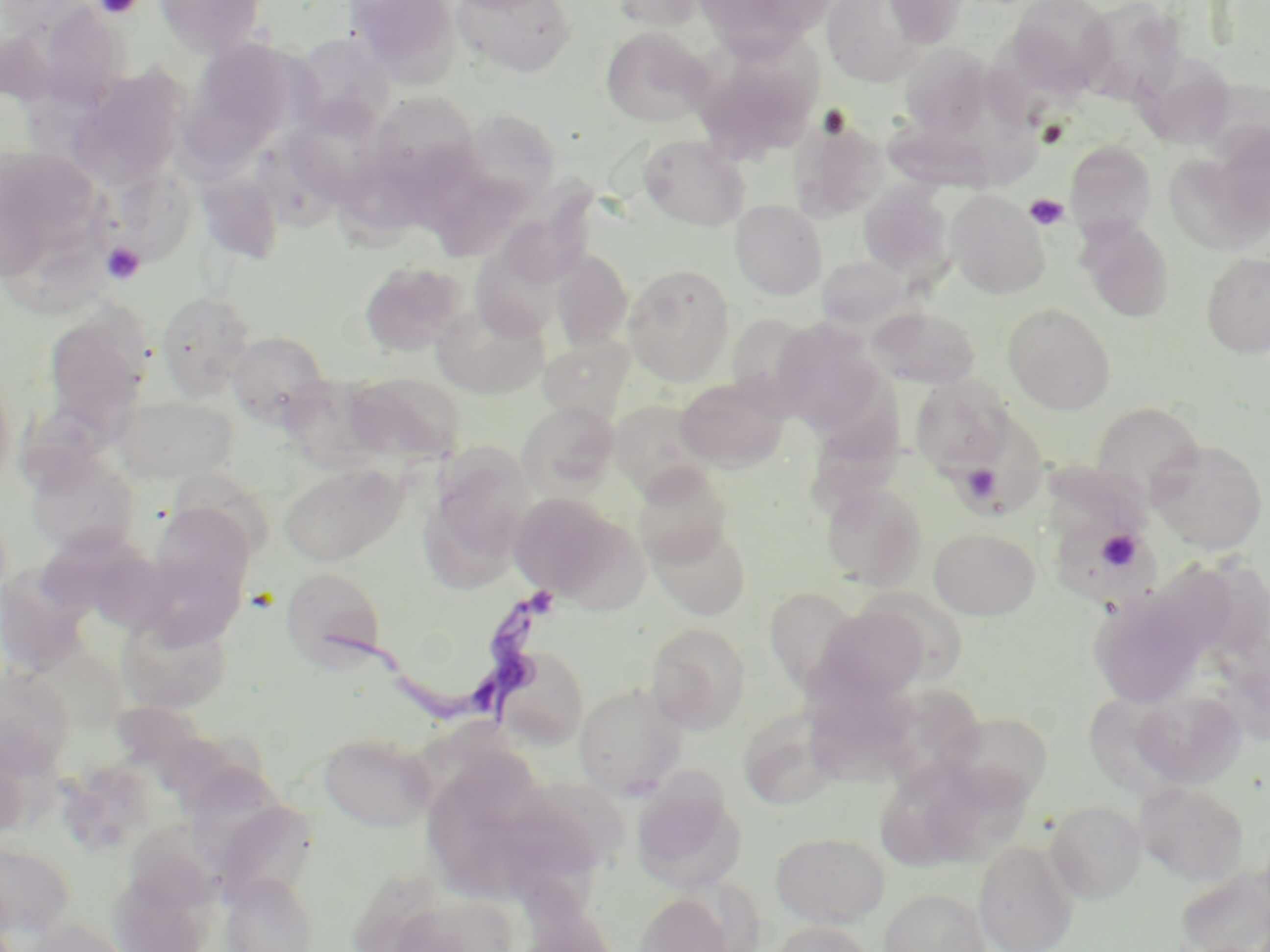
slide_level_diagnosis: Trypanosoma brucei
field_of_view: one of a larger specimen
magnification: 1000x
uninfected_red_blood_cell_locations: 'approximate bounding boxes as (x1, y1, x2, y2) in pixels: (153, 0, 267, 56), (345, 0, 462, 86), (452, 0, 576, 78), (611, 0, 707, 30), (694, 0, 829, 57), (821, 0, 925, 87), (884, 0, 971, 48), (1005, 0, 1115, 98), (1076, 0, 1185, 104), (600, 26, 711, 127), (691, 32, 825, 161), (290, 33, 395, 133), (192, 38, 307, 144), (899, 43, 997, 139), (1141, 58, 1237, 148), (71, 66, 190, 186), (365, 93, 481, 196), (284, 98, 388, 205), (459, 109, 560, 207), (790, 115, 890, 221), (638, 135, 750, 231), (1064, 141, 1157, 240), (0, 147, 109, 278), (1163, 151, 1264, 256), (109, 164, 197, 266), (197, 171, 285, 264), (858, 182, 954, 282), (947, 191, 1049, 298), (731, 200, 827, 300), (1078, 219, 1175, 322), (470, 236, 566, 342), (552, 250, 633, 350), (1201, 252, 1270, 358), (818, 256, 909, 330), (359, 261, 466, 356), (623, 264, 736, 386), (156, 291, 256, 398), (432, 303, 548, 399), (1004, 304, 1115, 413), (871, 306, 979, 389), (41, 307, 152, 439), (725, 313, 816, 406), (770, 318, 885, 434), (228, 331, 331, 427), (0, 362, 17, 490), (343, 373, 464, 468), (911, 375, 1016, 471), (675, 376, 789, 472), (113, 392, 239, 484), (802, 393, 907, 524), (609, 400, 714, 498), (518, 401, 620, 496), (1092, 401, 1205, 503), (1148, 440, 1268, 556), (426, 443, 534, 572), (24, 448, 140, 558), (278, 463, 406, 567), (631, 465, 731, 568), (174, 470, 274, 573), (820, 483, 927, 590), (509, 493, 634, 604), (147, 501, 255, 609), (650, 522, 751, 620), (1059, 522, 1163, 610), (929, 528, 1040, 620), (40, 533, 189, 634), (280, 566, 388, 671), (764, 587, 865, 694), (1089, 587, 1209, 709), (816, 604, 932, 706), (117, 608, 232, 713), (645, 623, 750, 733), (494, 645, 589, 749), (0, 667, 76, 775), (574, 683, 685, 799), (1131, 690, 1246, 788), (885, 691, 985, 792), (740, 711, 837, 811), (941, 711, 1053, 807), (318, 731, 436, 832), (428, 751, 550, 880), (631, 769, 745, 894), (506, 773, 628, 879), (1136, 782, 1249, 883), (1045, 800, 1146, 903), (216, 809, 320, 911), (125, 822, 222, 914), (771, 831, 890, 926), (0, 840, 76, 940), (974, 840, 1078, 952), (1174, 864, 1270, 952), (220, 872, 319, 952), (879, 888, 991, 952), (634, 892, 735, 951), (22, 918, 130, 952), (766, 921, 877, 952)'
stain: May-Grünwald-Giemsa
preparation: thin blood smear
trypanosoma_brucei_locations: 'approximate bounding boxes as (x1, y1, x2, y2) in pixels: (309, 582, 561, 734)'
image_size: 1270×952 pixels
platelet_locations: 'approximate bounding boxes as (x1, y1, x2, y2) in pixels: (94, 0, 144, 19), (1039, 121, 1067, 148), (1024, 193, 1070, 230), (102, 242, 146, 284), (961, 463, 1001, 504), (1096, 530, 1142, 571)'
modality: optical microscopy